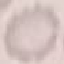
Malaria status: uninfected. Thin smear of blood. Giemsa stain. Automatically extracted cell patch, resized to 64 × 64 pixels. Photographed with a smartphone camera at the microscope eyepiece.